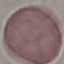

Summary:
  - Malaria status: uninfected
  - Image type: automatically extracted cell patch, resized to 64 × 64 pixels
  - Stain: Giemsa
  - Preparation: thin blood film
  - Capture: smartphone camera at the microscope eyepiece